Name the parasite shown.
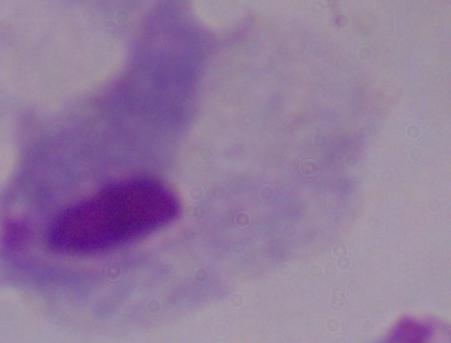

A trichomonad.

magnification = 1000x
modality = photomicrograph